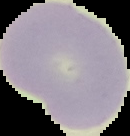

malaria status = uninfected
image type = segmented cell region with the area outside set to black
preparation = thin blood film
image size = 130×136 pixels